Report the malaria status of this cell.
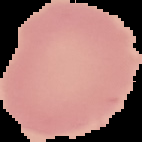

Uninfected.

image size = 142×142 pixels
image type = segmented cell region with the area outside set to black
preparation = thin blood smear